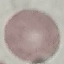
malaria_status: uninfected
preparation: thin blood smear
capture: smartphone camera at the microscope eyepiece
image_type: cell patch, automatically extracted from a larger field of view and resized to 64 × 64 pixels
stain: Giemsa